Report the malaria status of this cell.
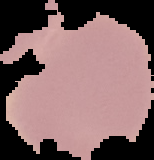

It is uninfected.

image size = 154×160 pixels
preparation = thin blood film
image type = cell region segmented out of the field of view; surrounding area masked to black